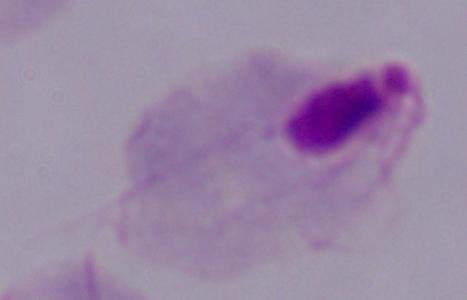
Summary:
  - Magnification: 1000x
  - Modality: photomicrograph
  - Identification: trichomonad